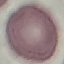
Summary:
  - Result: no malaria parasites seen
  - Image type: cell patch, automatically extracted from a larger field of view and resized to 64 × 64 pixels
  - Capture: smartphone camera at the microscope eyepiece
  - Stain: Giemsa
  - Preparation: thin blood smear